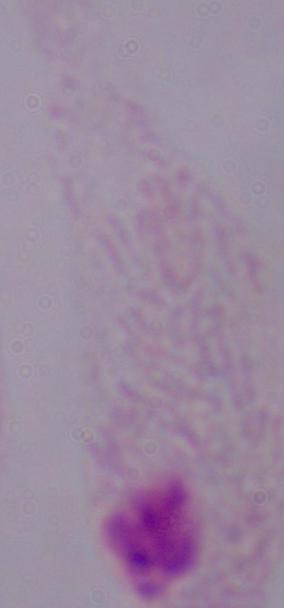
Photomicrograph. Captured at 1000x magnification. A trichomonad is seen.